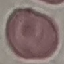

malaria status = uninfected
image type = automatically extracted cell patch, resized to 64 × 64 pixels
stain = Giemsa
capture = smartphone through the microscope eyepiece
preparation = thin blood smear